State the blood parasite species.
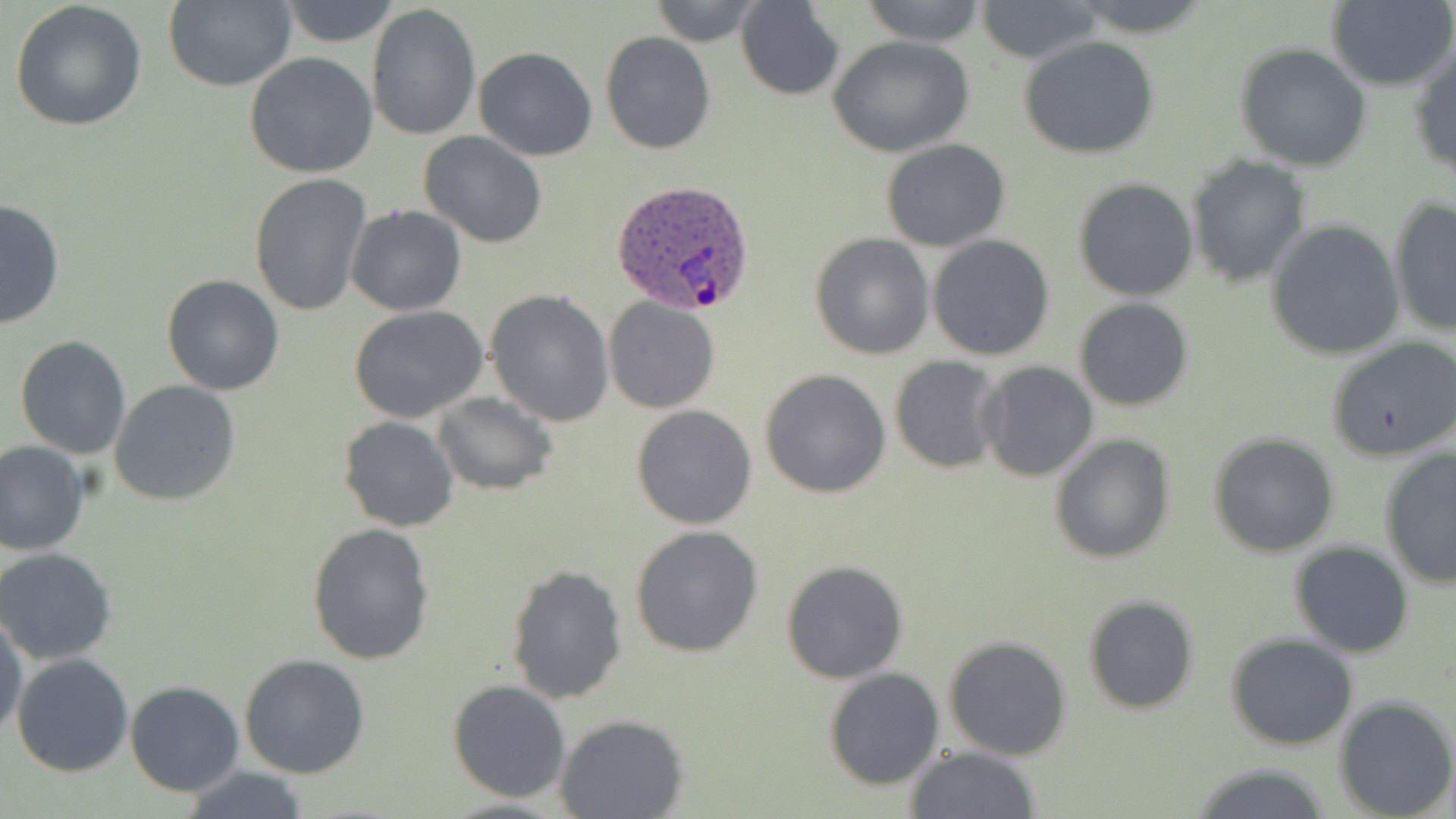

Plasmodium ovale.

Approximate bounding boxes as named x1/y1/x2/y2 corners in pixels. Plasmodium ovale-infected red blood cell locations: (x1=611, y1=180, x2=755, y2=315). Uninfected red blood cell locations: (x1=164, y1=0, x2=295, y2=92), (x1=277, y1=0, x2=405, y2=47), (x1=645, y1=0, x2=769, y2=46), (x1=858, y1=0, x2=988, y2=46), (x1=1070, y1=0, x2=1215, y2=37), (x1=1328, y1=0, x2=1456, y2=92), (x1=8, y1=2, x2=150, y2=134), (x1=735, y1=2, x2=843, y2=99), (x1=973, y1=2, x2=1105, y2=60), (x1=367, y1=3, x2=481, y2=143), (x1=601, y1=31, x2=714, y2=154), (x1=828, y1=35, x2=973, y2=157), (x1=1019, y1=37, x2=1159, y2=160), (x1=1234, y1=43, x2=1371, y2=171), (x1=1409, y1=43, x2=1456, y2=181), (x1=474, y1=46, x2=598, y2=161), (x1=244, y1=53, x2=377, y2=179), (x1=419, y1=131, x2=548, y2=247), (x1=881, y1=139, x2=1011, y2=251), (x1=1186, y1=155, x2=1311, y2=287), (x1=249, y1=174, x2=371, y2=316), (x1=1072, y1=177, x2=1199, y2=301), (x1=0, y1=196, x2=67, y2=329), (x1=1388, y1=197, x2=1455, y2=337), (x1=347, y1=205, x2=466, y2=315), (x1=1265, y1=220, x2=1406, y2=360), (x1=809, y1=233, x2=934, y2=360), (x1=927, y1=234, x2=1056, y2=360), (x1=162, y1=274, x2=285, y2=395), (x1=487, y1=290, x2=614, y2=427), (x1=604, y1=297, x2=719, y2=415), (x1=1073, y1=299, x2=1195, y2=411), (x1=350, y1=307, x2=488, y2=425), (x1=1327, y1=333, x2=1456, y2=455), (x1=14, y1=335, x2=131, y2=459), (x1=890, y1=357, x2=1005, y2=473), (x1=976, y1=362, x2=1100, y2=482), (x1=760, y1=369, x2=890, y2=497), (x1=109, y1=379, x2=241, y2=506), (x1=432, y1=394, x2=556, y2=496), (x1=631, y1=405, x2=758, y2=530), (x1=338, y1=418, x2=458, y2=533), (x1=1208, y1=432, x2=1340, y2=558), (x1=1050, y1=435, x2=1176, y2=563), (x1=0, y1=439, x2=90, y2=555), (x1=1379, y1=448, x2=1456, y2=591), (x1=307, y1=524, x2=435, y2=666), (x1=629, y1=525, x2=765, y2=659), (x1=1290, y1=541, x2=1415, y2=658), (x1=0, y1=546, x2=118, y2=664), (x1=782, y1=560, x2=907, y2=683), (x1=506, y1=564, x2=629, y2=705), (x1=1083, y1=595, x2=1199, y2=714), (x1=0, y1=611, x2=28, y2=744), (x1=1226, y1=634, x2=1359, y2=750), (x1=943, y1=635, x2=1072, y2=760), (x1=11, y1=653, x2=133, y2=776), (x1=240, y1=653, x2=370, y2=778), (x1=824, y1=667, x2=944, y2=789), (x1=448, y1=679, x2=573, y2=802), (x1=125, y1=681, x2=244, y2=797), (x1=1334, y1=696, x2=1456, y2=818), (x1=555, y1=714, x2=688, y2=819), (x1=904, y1=746, x2=1041, y2=819), (x1=1184, y1=764, x2=1336, y2=819), (x1=176, y1=766, x2=311, y2=819). Light microscopy. 1000x magnification. Image is 1456×819 pixels. Thin blood film. May-Grünwald-Giemsa stain. One field of a larger specimen.